Locate every Plasmodium falciparum-infected red blood cell.
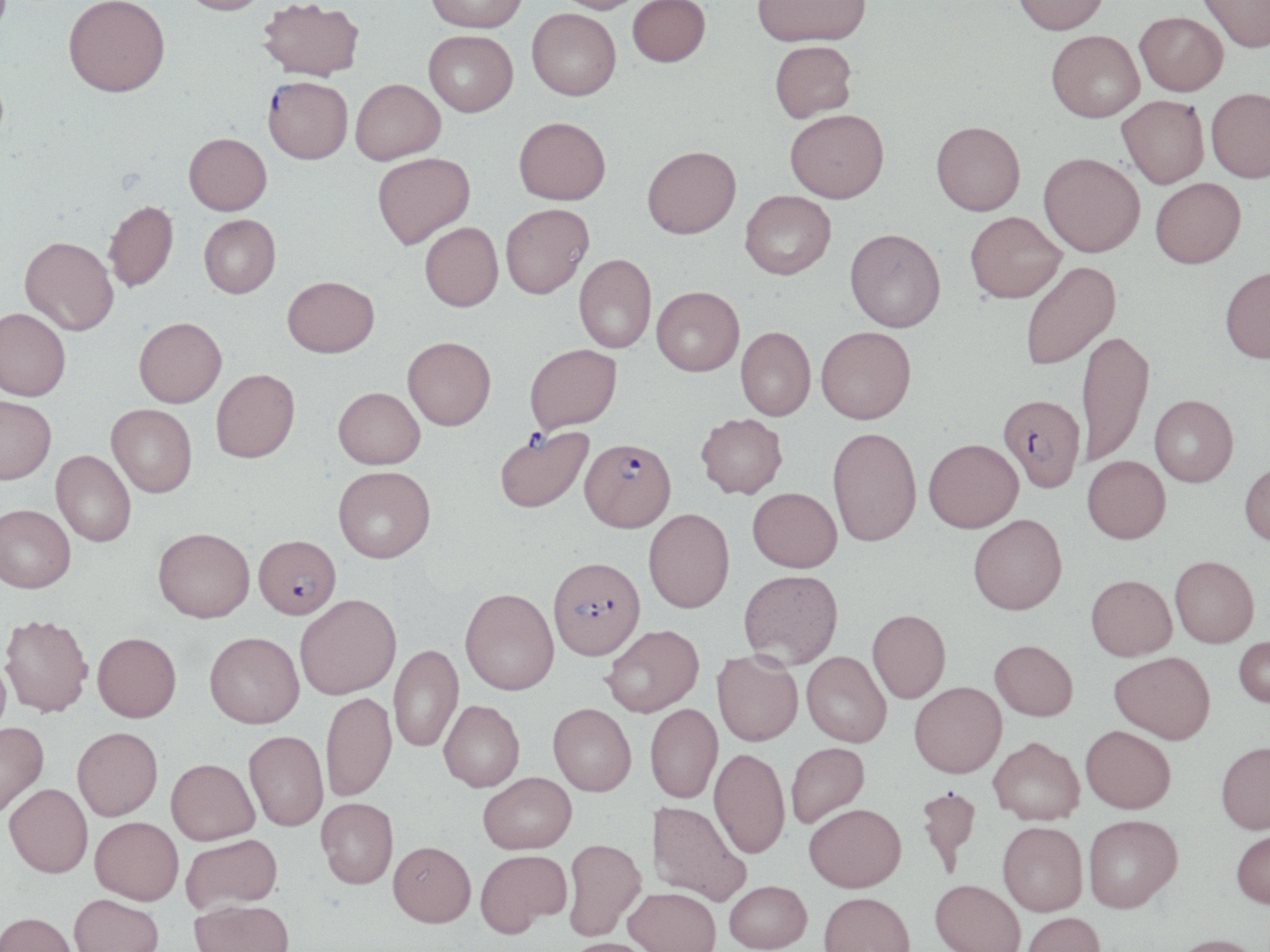
Approximate bounding boxes as named x1/y1/x2/y2 corners in pixels.
Plasmodium falciparum-infected red blood cells: (x1=263, y1=80, x2=353, y2=167), (x1=999, y1=398, x2=1084, y2=496), (x1=494, y1=425, x2=594, y2=516), (x1=580, y1=440, x2=676, y2=535), (x1=253, y1=535, x2=341, y2=620), (x1=548, y1=558, x2=645, y2=663).

Uninfected red blood cell locations: (x1=179, y1=0, x2=269, y2=19), (x1=427, y1=0, x2=527, y2=36), (x1=553, y1=0, x2=645, y2=16), (x1=628, y1=0, x2=710, y2=70), (x1=753, y1=0, x2=871, y2=51), (x1=1012, y1=0, x2=1110, y2=39), (x1=1198, y1=0, x2=1270, y2=56), (x1=64, y1=2, x2=170, y2=103), (x1=258, y1=2, x2=364, y2=85), (x1=527, y1=12, x2=621, y2=104), (x1=1135, y1=15, x2=1227, y2=100), (x1=423, y1=33, x2=518, y2=120), (x1=1046, y1=34, x2=1144, y2=126), (x1=770, y1=44, x2=858, y2=126), (x1=351, y1=82, x2=446, y2=168), (x1=1206, y1=92, x2=1270, y2=186), (x1=1116, y1=98, x2=1209, y2=191), (x1=785, y1=115, x2=889, y2=207), (x1=513, y1=121, x2=611, y2=209), (x1=931, y1=126, x2=1025, y2=219), (x1=183, y1=136, x2=271, y2=218), (x1=642, y1=150, x2=741, y2=243), (x1=373, y1=155, x2=476, y2=253), (x1=1038, y1=157, x2=1144, y2=261), (x1=1151, y1=181, x2=1246, y2=273), (x1=740, y1=194, x2=836, y2=283), (x1=104, y1=203, x2=179, y2=294), (x1=501, y1=206, x2=594, y2=303), (x1=965, y1=215, x2=1066, y2=307), (x1=199, y1=217, x2=281, y2=300), (x1=420, y1=225, x2=504, y2=315), (x1=844, y1=233, x2=946, y2=336), (x1=19, y1=239, x2=119, y2=337), (x1=574, y1=257, x2=656, y2=355), (x1=1022, y1=262, x2=1122, y2=372), (x1=1221, y1=271, x2=1270, y2=367), (x1=283, y1=278, x2=380, y2=360), (x1=651, y1=290, x2=744, y2=380), (x1=1, y1=309, x2=71, y2=402), (x1=134, y1=318, x2=227, y2=409), (x1=735, y1=329, x2=815, y2=423), (x1=815, y1=330, x2=916, y2=428), (x1=1077, y1=332, x2=1155, y2=470), (x1=403, y1=339, x2=496, y2=433), (x1=525, y1=347, x2=623, y2=436), (x1=211, y1=369, x2=301, y2=463), (x1=333, y1=388, x2=425, y2=469), (x1=0, y1=396, x2=56, y2=484), (x1=1149, y1=398, x2=1238, y2=489), (x1=106, y1=404, x2=197, y2=497), (x1=696, y1=414, x2=787, y2=500), (x1=827, y1=429, x2=921, y2=549), (x1=924, y1=440, x2=1023, y2=534), (x1=51, y1=450, x2=136, y2=546), (x1=1082, y1=457, x2=1170, y2=545), (x1=1239, y1=460, x2=1270, y2=548), (x1=333, y1=466, x2=435, y2=562), (x1=747, y1=487, x2=842, y2=574), (x1=0, y1=504, x2=76, y2=592), (x1=644, y1=509, x2=735, y2=614), (x1=968, y1=514, x2=1067, y2=615), (x1=153, y1=527, x2=254, y2=622), (x1=1170, y1=556, x2=1259, y2=648), (x1=738, y1=570, x2=843, y2=670), (x1=1085, y1=575, x2=1177, y2=661), (x1=460, y1=589, x2=559, y2=695), (x1=295, y1=593, x2=401, y2=699), (x1=867, y1=609, x2=950, y2=704), (x1=0, y1=614, x2=92, y2=717), (x1=602, y1=625, x2=704, y2=717), (x1=92, y1=632, x2=181, y2=722), (x1=205, y1=632, x2=304, y2=727), (x1=1234, y1=635, x2=1270, y2=708), (x1=990, y1=639, x2=1078, y2=720), (x1=389, y1=644, x2=463, y2=752), (x1=712, y1=650, x2=803, y2=747), (x1=1109, y1=651, x2=1215, y2=744), (x1=0, y1=652, x2=12, y2=745), (x1=802, y1=652, x2=891, y2=747), (x1=909, y1=681, x2=1006, y2=778), (x1=321, y1=692, x2=396, y2=801), (x1=439, y1=700, x2=524, y2=791), (x1=548, y1=703, x2=636, y2=797), (x1=645, y1=704, x2=723, y2=804), (x1=0, y1=722, x2=49, y2=817), (x1=1081, y1=725, x2=1175, y2=813), (x1=73, y1=726, x2=163, y2=821), (x1=244, y1=730, x2=328, y2=831), (x1=988, y1=737, x2=1084, y2=825), (x1=786, y1=742, x2=870, y2=828), (x1=1216, y1=743, x2=1270, y2=835), (x1=709, y1=748, x2=790, y2=859), (x1=166, y1=758, x2=259, y2=844), (x1=478, y1=772, x2=576, y2=853), (x1=4, y1=783, x2=93, y2=877), (x1=916, y1=784, x2=982, y2=878), (x1=316, y1=798, x2=398, y2=888), (x1=646, y1=800, x2=749, y2=905), (x1=804, y1=803, x2=906, y2=892), (x1=1082, y1=815, x2=1182, y2=913), (x1=90, y1=817, x2=183, y2=904), (x1=998, y1=822, x2=1088, y2=916), (x1=1231, y1=827, x2=1270, y2=909), (x1=181, y1=833, x2=282, y2=913), (x1=562, y1=838, x2=646, y2=941), (x1=388, y1=841, x2=475, y2=927), (x1=475, y1=849, x2=571, y2=935), (x1=930, y1=879, x2=1025, y2=952), (x1=724, y1=880, x2=812, y2=952), (x1=624, y1=887, x2=721, y2=952), (x1=819, y1=892, x2=915, y2=952), (x1=70, y1=894, x2=164, y2=952), (x1=190, y1=899, x2=295, y2=952), (x1=0, y1=911, x2=78, y2=952), (x1=1022, y1=912, x2=1105, y2=952), (x1=1169, y1=934, x2=1265, y2=952), (x1=563, y1=937, x2=659, y2=952). Slide-level diagnosis: Plasmodium falciparum. One field of a larger specimen. Captured at 1000x magnification. Light microscopy. Image is 1270×952 pixels. May-Grünwald-Giemsa stain. Thin blood film.